Report the malaria status of this cell.
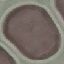

It is uninfected.

Summary:
  - Stain: Giemsa
  - Capture: smartphone through the microscope eyepiece
  - Preparation: thin blood film
  - Image type: automatically extracted cell patch, resized to 64 × 64 pixels